Point out each Plasmodium parasite.
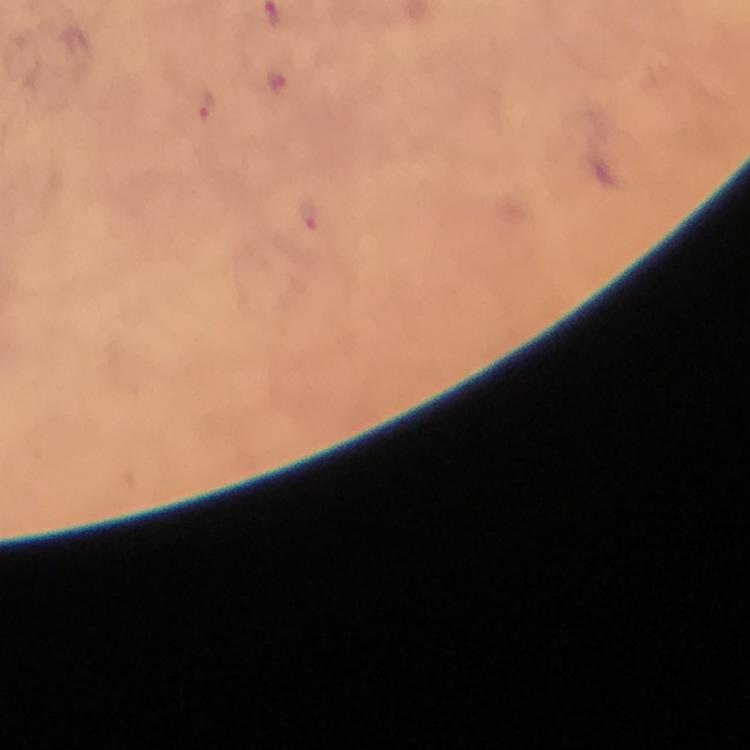

Approximate centers as [x, y] in pixels.
Plasmodium parasites: [205, 101], [307, 217].

stain = Giemsa
immersion oil = applied
context = from a malaria diagnostic workup
capture = smartphone mounted on the microscope
magnification = 100x
preparation = thick blood film
cropped from = a single field of view
image size = 750×750 pixels